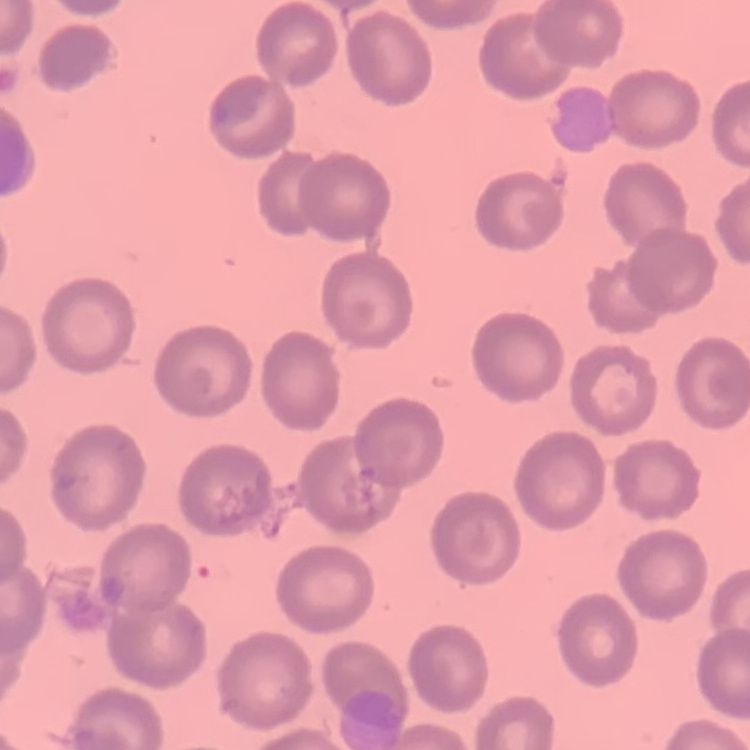
erythrocyte morphology = no rouleaux formation
preparation = thin blood film
image type = square crop of a larger photomicrograph
stain = Field's or Giemsa